Classify this cell by malaria status.
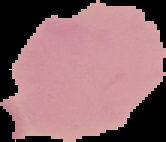

It is uninfected.

From a thin blood smear. The area outside the segmented cell region is set to black. Image is 166×142 pixels.